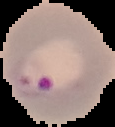
Summary:
  - Image size: 115×127 pixels
  - Image type: segmented cell region with the area outside set to black
  - Preparation: thin blood smear
  - Malaria status: parasitized